Classify this cell by malaria status.
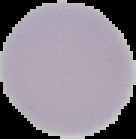

Uninfected.

Summary:
  - Image type: segmented cell region with the area outside set to black
  - Preparation: thin blood film
  - Image size: 136×139 pixels